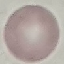
malaria_status: uninfected
capture: smartphone through the microscope eyepiece
preparation: thin blood film
image_type: cell patch, automatically extracted from a larger field of view and resized to 64 × 64 pixels
stain: Giemsa